Outline malaria parasites and classify them by life-cycle stage.
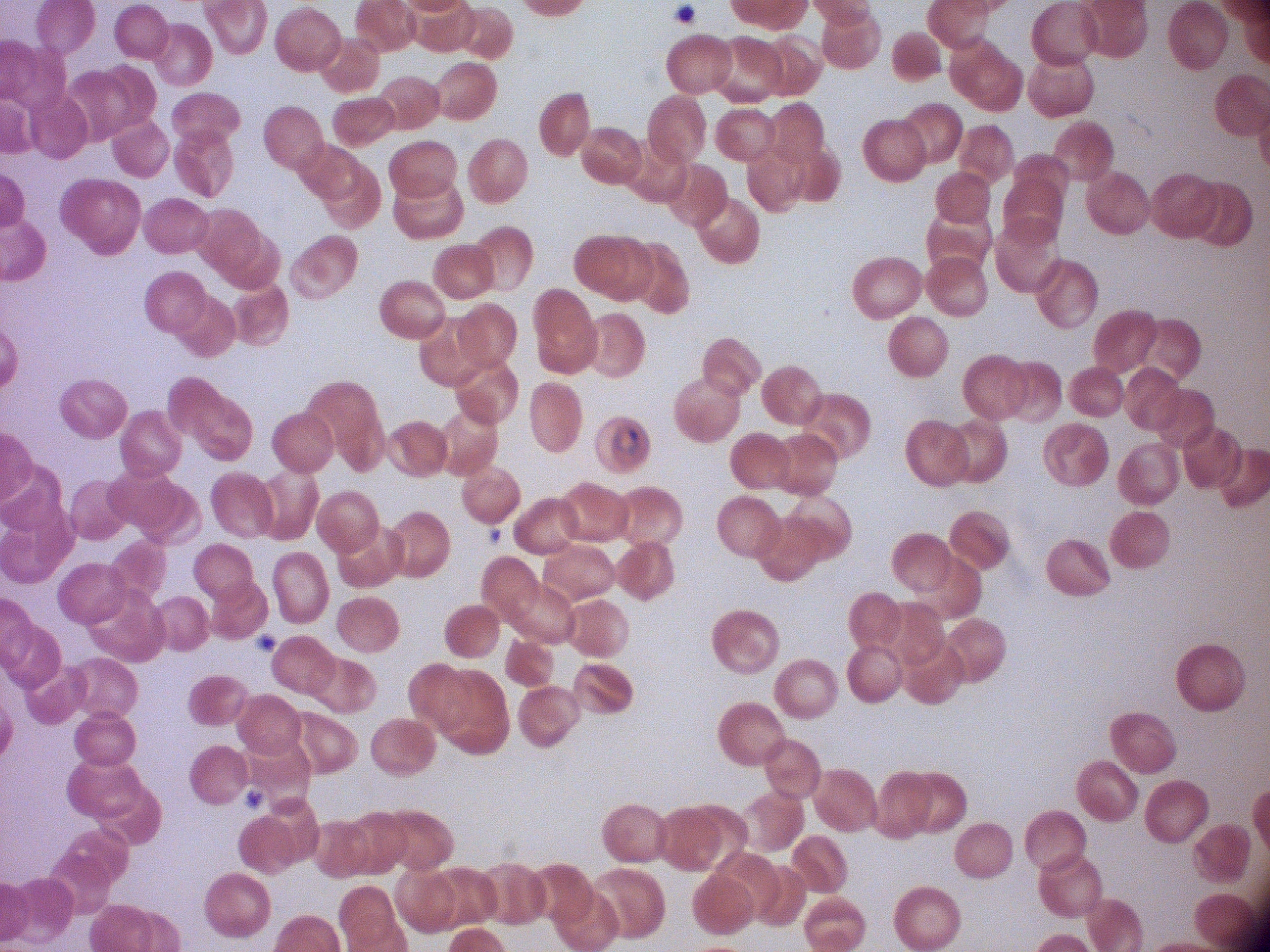
Approximate bounding boxes as (x1,y1)-(x2,y2) corner pairs in pixels, from the source annotation, which is not necessarily exhaustive.
Ring forms: (603,416)-(646,458).

Summary:
  - Stain: Giemsa
  - Preparation: thin blood film
  - Species: Plasmodium falciparum
  - Magnification: 100x
  - Microscope: Leica DM2000 with built-in camera
  - Field of view: single
  - Image size: 1270×952 pixels